Locate every malaria parasite.
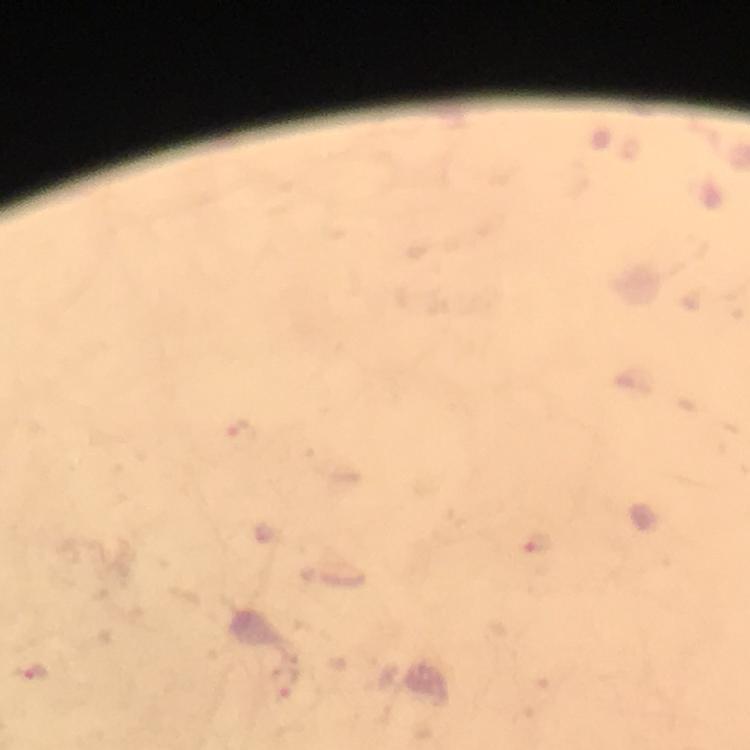
Approximate centers as (x, y) in pixels.
Malaria parasites: (539, 546), (30, 672), (284, 683).

Summary:
  - Immersion oil: applied
  - Capture: smartphone mounted on the microscope
  - Magnification: 100x
  - Cropped from: a single field of view
  - Preparation: thick blood smear
  - Context: from a diagnostic examination for malaria
  - Stain: Giemsa
  - Image size: 750×750 pixels